Assess for parasitized red blood cells.
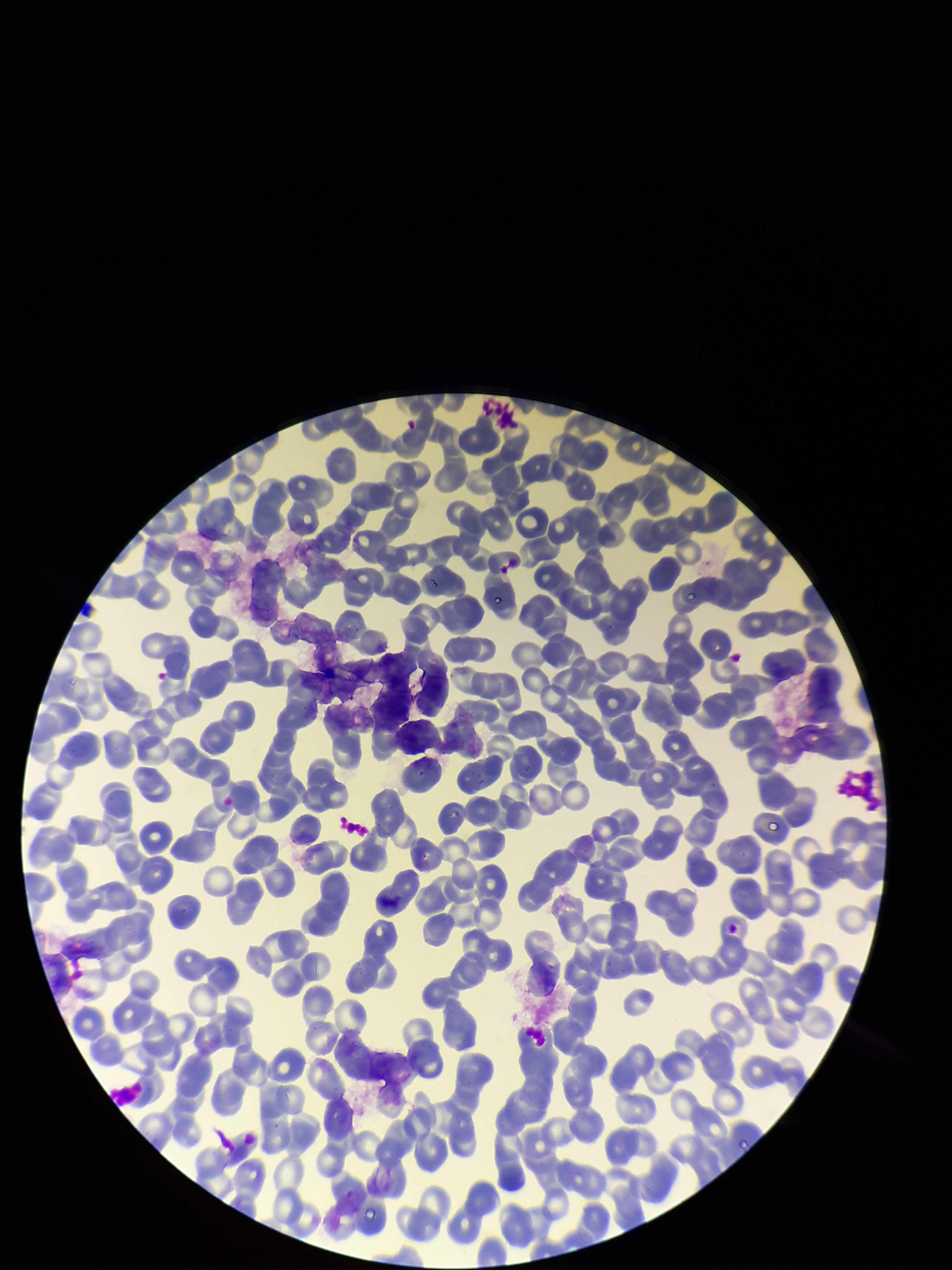

None seen.

Image is 952×1270 pixels. Smartphone photograph taken through the eyepiece of a microscope. Parasitized red blood cell count: 0. Patient malaria status: negative. Red blood cell count: 218. One field from this slide. Preparation: thin. Giemsa stain.